State which parasite is depicted.
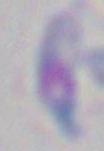
This is Toxoplasma gondii.

Summary:
  - Magnification: 1000x
  - Modality: micrograph